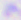
Captured at 400x magnification. Toxoplasma gondii is seen. Micrograph.